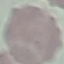
malaria status = uninfected
capture = smartphone camera at the microscope eyepiece
stain = Giemsa
image type = cell patch, automatically extracted from a larger field of view and resized to 64 × 64 pixels
preparation = thin blood film